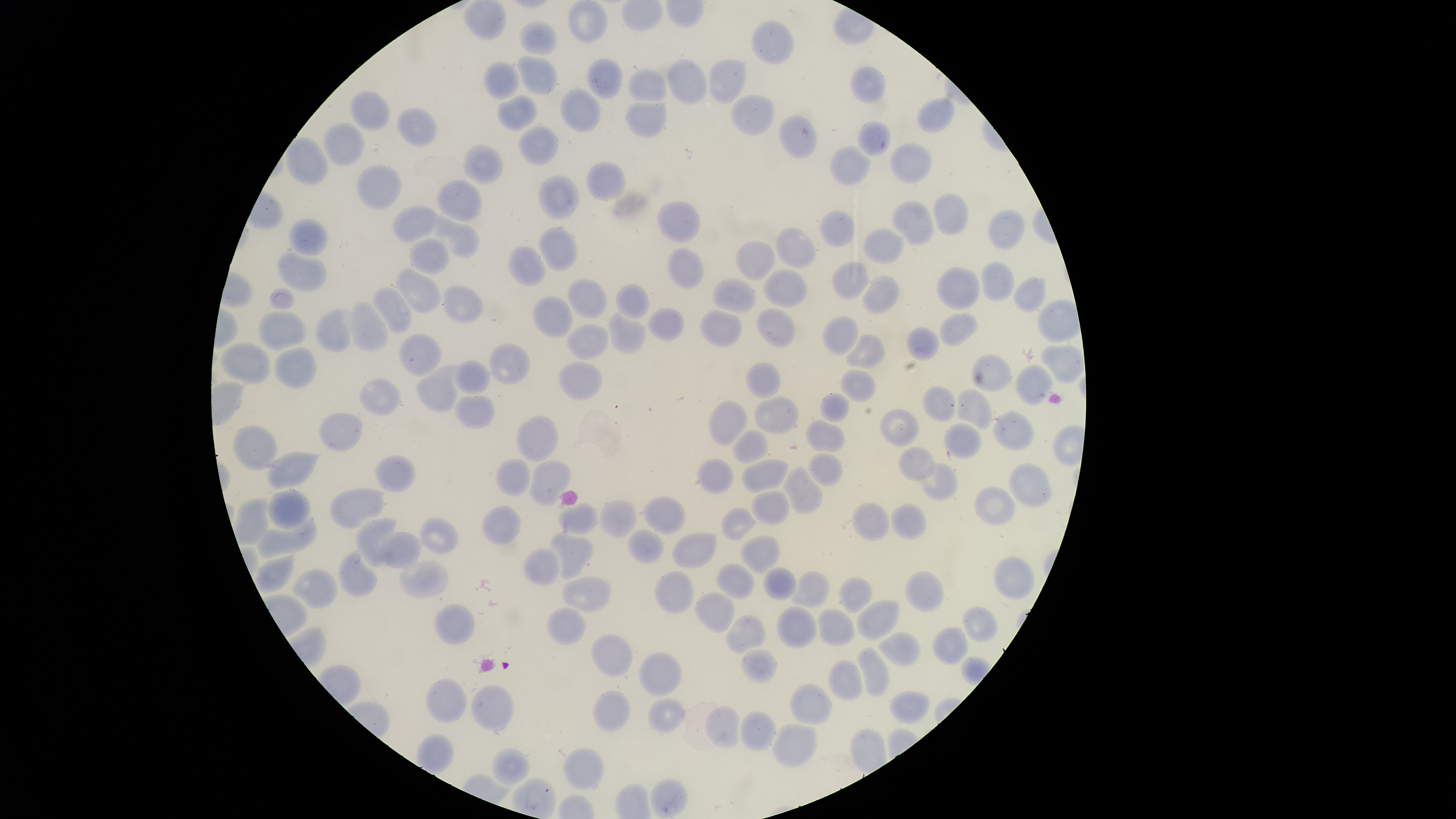
capture = smartphone photograph through the microscope eyepiece
presence = no malaria parasites identified
field of view = single
stain = Giemsa
uninfected red blood cells = approximate bounding boxes as [left, top, right, bottom] in pixels: [463, 0, 507, 40], [567, 0, 608, 44], [751, 19, 794, 66], [519, 20, 558, 56], [517, 54, 558, 95], [586, 58, 623, 99], [708, 58, 748, 104], [668, 59, 707, 105], [482, 60, 521, 98], [850, 65, 886, 104], [628, 69, 668, 102], [559, 87, 601, 133], [350, 90, 390, 131], [730, 94, 775, 137], [497, 95, 538, 130], [916, 97, 956, 133], [624, 100, 667, 138], [396, 107, 438, 148], [778, 115, 818, 159], [856, 120, 891, 157], [322, 122, 365, 166], [518, 125, 559, 166], [285, 137, 329, 185], [889, 142, 933, 185], [462, 143, 504, 185], [829, 145, 871, 186], [586, 162, 628, 201], [356, 163, 401, 210], [538, 174, 580, 220], [436, 178, 483, 221], [932, 194, 969, 236], [656, 200, 701, 243], [891, 200, 935, 246], [392, 205, 440, 243], [987, 209, 1025, 249], [819, 210, 855, 248], [434, 213, 480, 259], [288, 217, 328, 257], [538, 226, 578, 271], [775, 227, 817, 269], [862, 228, 904, 264], [408, 237, 449, 275], [735, 240, 776, 281], [508, 245, 546, 287], [667, 246, 704, 289], [277, 250, 327, 291], [980, 260, 1015, 302], [831, 261, 870, 301], [395, 266, 443, 313], [937, 267, 980, 310], [763, 269, 809, 309], [862, 274, 900, 315], [1013, 276, 1046, 313], [712, 277, 757, 315], [566, 278, 608, 318], [615, 283, 649, 320], [442, 285, 485, 323], [371, 287, 412, 333], [532, 295, 573, 339], [351, 300, 389, 352], [647, 307, 685, 342], [756, 307, 795, 349], [315, 308, 357, 353], [700, 309, 742, 348], [258, 310, 306, 350], [607, 311, 647, 354], [939, 312, 977, 346], [823, 315, 859, 356], [566, 322, 609, 360], [906, 326, 940, 360], [398, 332, 442, 376], [845, 333, 886, 368], [221, 342, 271, 383], [488, 342, 531, 385], [1038, 344, 1084, 384], [273, 346, 317, 389], [970, 354, 1012, 392], [453, 360, 490, 394], [558, 362, 601, 401], [746, 362, 781, 399], [415, 364, 462, 412], [1015, 364, 1054, 405], [840, 369, 876, 403], [359, 377, 401, 416], [923, 385, 956, 422], [956, 388, 993, 430], [820, 392, 850, 422], [453, 395, 496, 429], [754, 396, 799, 435], [708, 400, 748, 446], [879, 408, 919, 447], [992, 410, 1035, 452], [319, 411, 364, 452], [516, 415, 559, 463], [806, 419, 846, 452], [943, 423, 983, 459], [232, 425, 278, 470], [732, 429, 769, 465], [898, 447, 936, 481], [267, 451, 323, 490], [808, 452, 842, 486], [375, 454, 416, 493], [696, 458, 735, 495], [741, 458, 789, 493], [495, 459, 532, 497], [529, 459, 571, 507], [921, 462, 959, 501], [1008, 463, 1054, 508], [783, 465, 823, 515], [973, 485, 1017, 526], [329, 488, 386, 530], [267, 489, 312, 530], [751, 490, 790, 526], [642, 496, 686, 535], [232, 498, 270, 546], [598, 500, 638, 538], [558, 502, 599, 536], [851, 503, 891, 542], [890, 503, 927, 540], [482, 505, 522, 545], [721, 507, 757, 541], [254, 516, 318, 559], [355, 516, 397, 568], [419, 517, 459, 554], [627, 528, 665, 565], [379, 531, 422, 569], [550, 531, 594, 580], [671, 532, 717, 568], [738, 535, 781, 575], [523, 548, 561, 587], [338, 549, 379, 598], [254, 552, 295, 593], [993, 556, 1034, 599], [399, 559, 449, 599], [715, 564, 755, 600], [763, 566, 797, 600], [291, 569, 338, 609], [904, 569, 945, 613], [654, 570, 694, 614], [790, 570, 830, 608], [561, 575, 612, 613], [838, 577, 873, 613], [694, 592, 736, 633], [856, 599, 901, 640], [434, 603, 475, 645], [775, 606, 818, 649], [961, 606, 998, 642], [547, 607, 586, 646], [818, 608, 857, 646], [725, 614, 765, 656], [932, 626, 968, 665], [876, 631, 921, 667], [590, 634, 633, 678], [855, 646, 890, 698], [741, 648, 777, 684], [638, 652, 682, 697], [828, 659, 864, 702], [425, 678, 467, 724], [789, 683, 833, 725], [470, 684, 514, 735], [592, 690, 631, 733], [889, 691, 930, 724], [648, 697, 687, 734], [704, 705, 741, 749], [739, 710, 777, 751], [771, 723, 817, 768], [562, 747, 605, 790], [491, 748, 530, 787], [649, 778, 688, 818]
preparation = thin blood film
visible region = circular
image size = 1456×819 pixels